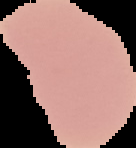
Result: negative for malaria parasites. Image is 136×148 pixels. The area outside the segmented cell region is set to black. From a thin blood film.